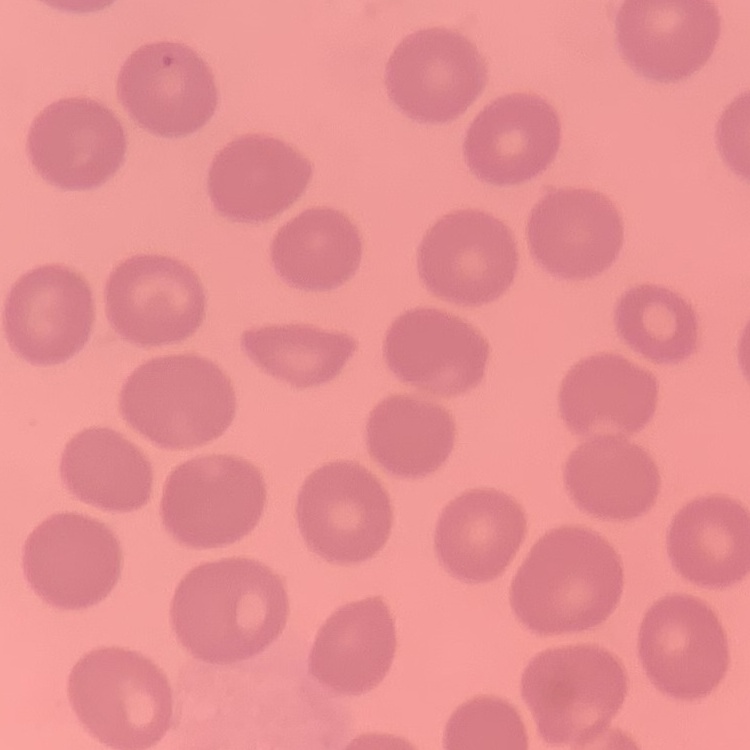

Summary:
  - Red blood cell morphology: no rouleaux formation
  - Stain: Field's or Giemsa
  - Image type: one tile cut from a larger photomicrograph
  - Preparation: thin blood film